State which parasite is depicted.
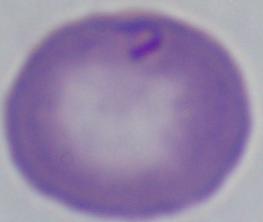

This is Babesia.

Summary:
  - Modality: photomicrograph
  - Magnification: 1000x